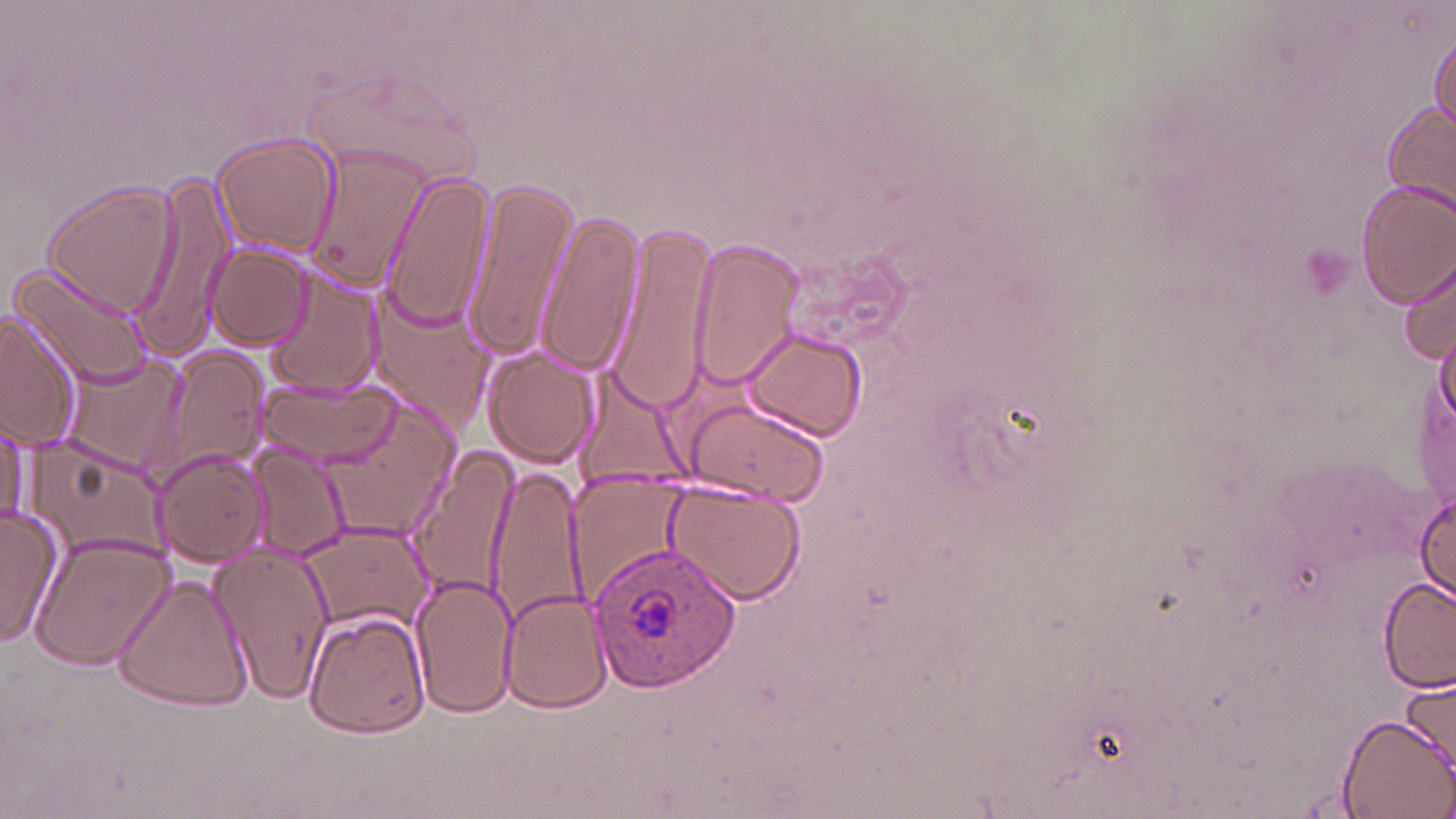 Approximate bounding boxes as named x1/y1/x2/y2 corners in pixels. Plasmodium ovale-infected red blood cell locations: (x1=589, y1=544, x2=743, y2=693). Platelet locations: (x1=1297, y1=246, x2=1353, y2=306). Uninfected red blood cell locations: (x1=1428, y1=28, x2=1455, y2=142), (x1=1379, y1=102, x2=1455, y2=221), (x1=212, y1=133, x2=340, y2=256), (x1=302, y1=145, x2=439, y2=295), (x1=378, y1=173, x2=496, y2=334), (x1=125, y1=178, x2=235, y2=361), (x1=461, y1=178, x2=579, y2=359), (x1=41, y1=180, x2=182, y2=321), (x1=1356, y1=180, x2=1456, y2=307), (x1=540, y1=209, x2=644, y2=376), (x1=606, y1=221, x2=719, y2=410), (x1=685, y1=238, x2=806, y2=390), (x1=204, y1=242, x2=314, y2=350), (x1=1400, y1=256, x2=1455, y2=367), (x1=11, y1=260, x2=156, y2=391), (x1=267, y1=273, x2=383, y2=401), (x1=368, y1=293, x2=494, y2=429), (x1=1, y1=309, x2=87, y2=452), (x1=1434, y1=324, x2=1455, y2=428), (x1=740, y1=328, x2=867, y2=443), (x1=140, y1=346, x2=271, y2=491), (x1=484, y1=348, x2=601, y2=468), (x1=61, y1=353, x2=188, y2=473), (x1=572, y1=371, x2=691, y2=495), (x1=257, y1=376, x2=405, y2=469), (x1=680, y1=395, x2=829, y2=506), (x1=321, y1=405, x2=457, y2=541), (x1=0, y1=417, x2=33, y2=529), (x1=24, y1=439, x2=169, y2=568), (x1=247, y1=443, x2=351, y2=564), (x1=404, y1=443, x2=524, y2=602), (x1=154, y1=448, x2=271, y2=568), (x1=485, y1=466, x2=589, y2=629), (x1=566, y1=474, x2=693, y2=606), (x1=662, y1=480, x2=806, y2=608), (x1=1415, y1=490, x2=1455, y2=601), (x1=0, y1=504, x2=63, y2=648), (x1=298, y1=524, x2=433, y2=638), (x1=31, y1=531, x2=175, y2=671), (x1=205, y1=543, x2=331, y2=703), (x1=411, y1=573, x2=516, y2=720), (x1=113, y1=575, x2=255, y2=714), (x1=1377, y1=579, x2=1455, y2=691), (x1=498, y1=588, x2=613, y2=714), (x1=302, y1=609, x2=434, y2=739), (x1=1401, y1=670, x2=1456, y2=779), (x1=1335, y1=714, x2=1454, y2=819). Slide-level diagnosis: Plasmodium ovale. 1000x magnification. Thin blood film. Image is 1456×819 pixels. May-Grünwald-Giemsa-stained preparation. Single field of view. Optical microscopy.